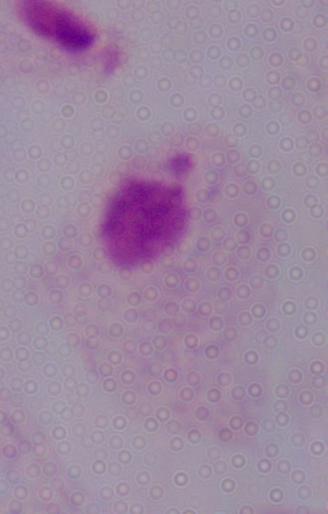
Summary:
  - Magnification: 1000x
  - Identification: trichomonad
  - Modality: micrograph